Report the malaria status of this cell.
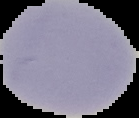
Uninfected.

{
  "image_type": "cell region segmented out of the field of view; surrounding area masked to black",
  "preparation": "thin blood smear",
  "image_size": "139×118 pixels"
}